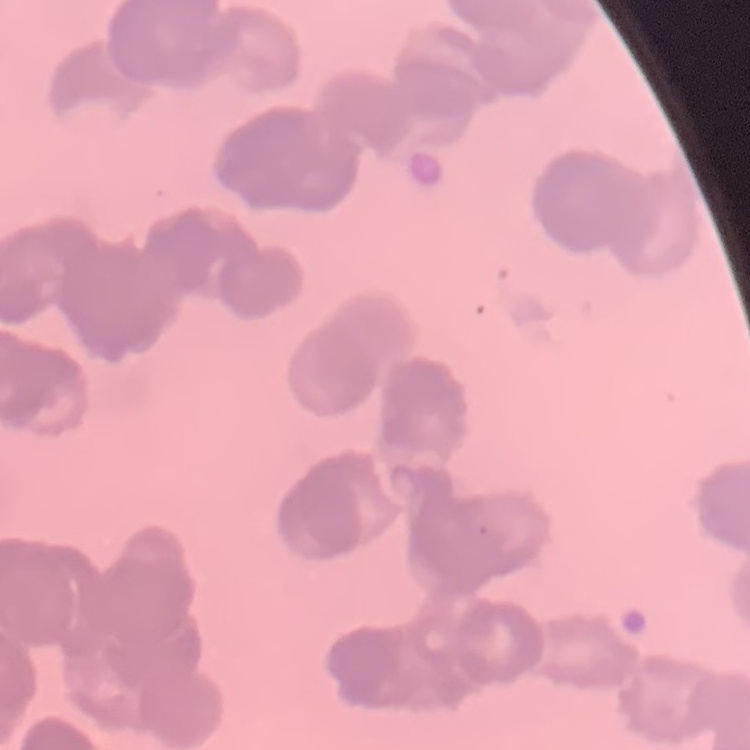 The red blood cells exhibit rouleaux formation. Thin blood smear. Field's or Giemsa stain. Square crop of a larger photomicrograph.